Outline each blood parasite and name the species.
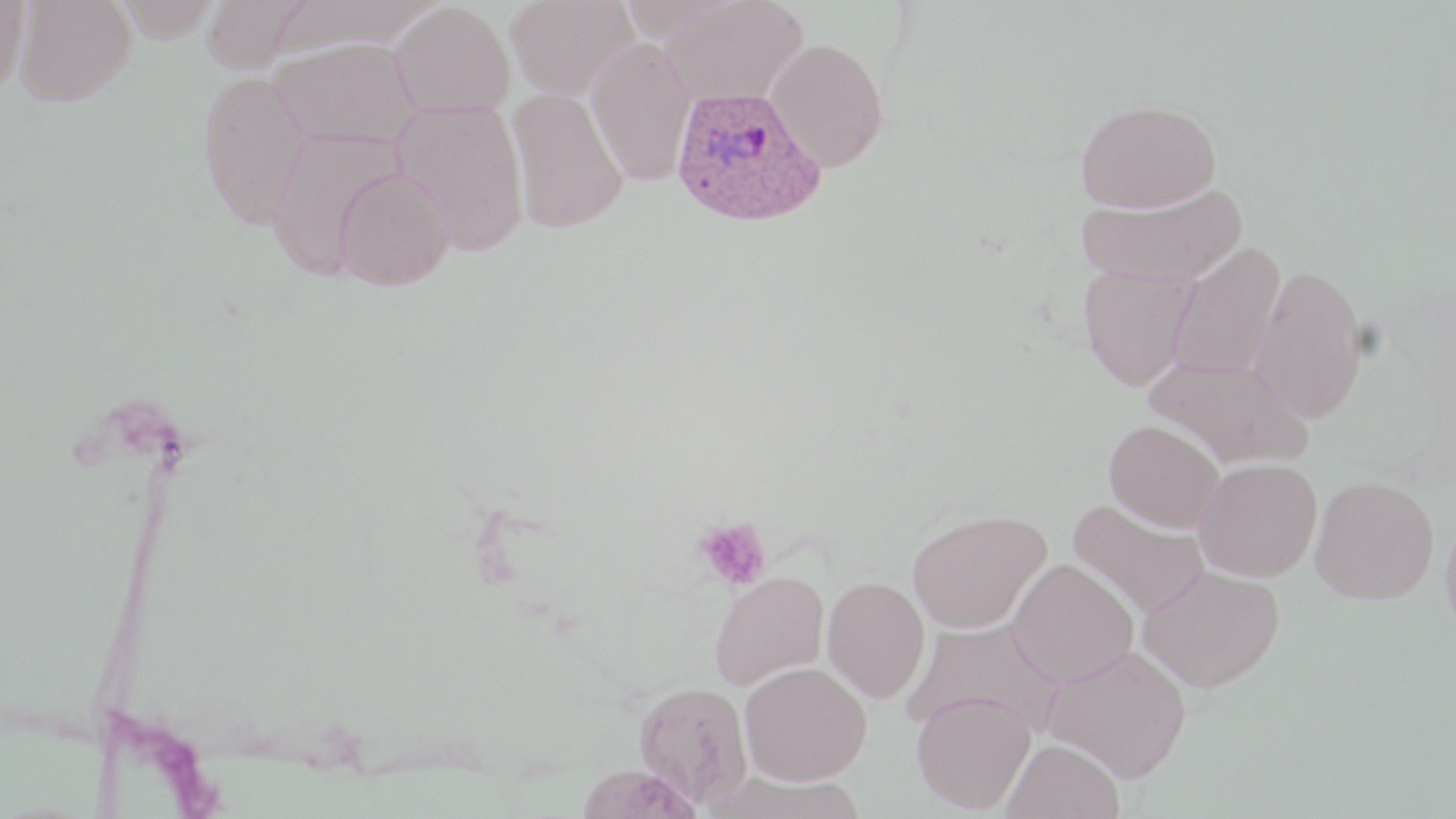

Approximate bounding boxes as [x1, y1, x2, y2] in pixels.
Plasmodium ovale-infected red blood cells: [670, 85, 826, 228].
No Plasmodium falciparum, Plasmodium malariae, Plasmodium vivax, Babesia divergens, or Trypanosoma brucei observed.

Uninfected red blood cell locations: [14, 0, 135, 106], [113, 0, 221, 42], [202, 0, 312, 73], [506, 0, 638, 100], [659, 0, 808, 107], [0, 1, 30, 92], [264, 1, 441, 58], [389, 1, 515, 117], [271, 36, 423, 150], [766, 37, 890, 172], [586, 39, 697, 187], [195, 69, 314, 230], [506, 88, 628, 234], [391, 98, 530, 256], [1074, 98, 1222, 213], [265, 126, 406, 280], [333, 168, 454, 291], [1076, 184, 1247, 286], [1166, 242, 1286, 381], [1247, 263, 1370, 424], [1078, 264, 1201, 392], [1145, 356, 1312, 469], [1103, 419, 1224, 533], [1193, 458, 1322, 582], [1310, 475, 1439, 604], [1068, 498, 1210, 618], [907, 508, 1051, 633], [1439, 510, 1456, 649], [1007, 559, 1138, 687], [1138, 564, 1285, 692], [708, 571, 829, 689], [822, 576, 930, 702], [904, 617, 1064, 740], [1043, 644, 1192, 783], [739, 661, 872, 784], [634, 681, 753, 808], [911, 690, 1036, 813], [1000, 738, 1125, 819], [574, 764, 703, 819]. Platelet locations: [693, 516, 772, 591]. Slide-level diagnosis: Plasmodium ovale. Captured at 1000x magnification. Single field of view. Image is 1456×819 pixels. May-Grünwald-Giemsa stain. Thin blood smear. Light microscopy.